Give the position of every malaria parasite and every leukocyte.
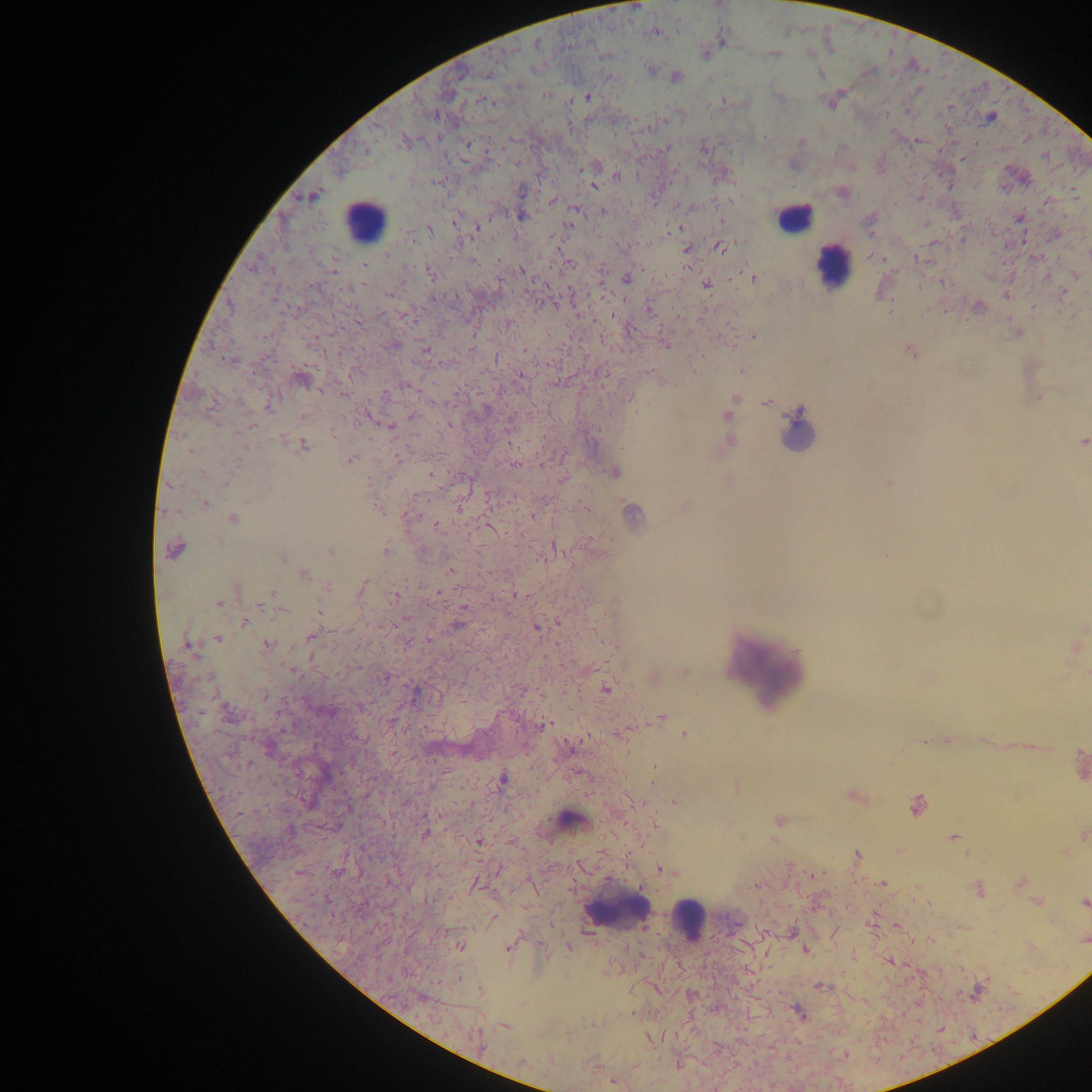
Approximate centers as x y in pixels.
Malaria parasites: 635 7; 655 32; 723 40; 537 44; 705 53; 810 53; 775 54; 650 69; 820 74; 676 77; 918 90; 547 95; 778 96; 588 97; 484 101; 830 103; 990 118; 800 142; 468 144; 618 177; 594 185; 522 191; 842 192; 311 196; 681 205; 575 209; 602 212; 522 216; 457 221; 870 224; 568 226; 478 227; 674 228; 429 230; 720 247; 686 251; 388 254; 473 261; 569 263; 364 265; 333 271; 430 272; 522 272; 1076 275; 626 278; 753 278; 943 283; 706 284; 390 293; 1006 295; 230 307; 406 316; 358 321; 509 324; 752 336; 396 345; 665 345; 425 349; 526 350; 912 351; 497 358; 230 361; 302 380; 519 380; 405 385; 344 396; 1038 398; 734 399; 240 402; 766 402; 270 406; 727 415; 412 416; 302 417; 251 426; 387 426; 282 440; 730 441; 1082 443; 303 445; 190 451; 400 458; 351 459; 515 464; 615 471; 202 472; 430 474; 728 480; 225 482; 369 482; 888 482; 204 503; 460 507; 685 507; 377 509; 632 513; 233 519; 438 526; 174 549; 330 551; 386 552; 282 558; 449 571; 304 575; 327 588; 361 588; 238 590; 438 592; 272 593; 396 595; 516 595; 219 603; 463 607; 318 611; 244 623; 457 625; 537 627; 310 637; 218 639; 428 640; 268 644; 187 645; 1077 646; 293 671; 685 671; 385 677; 654 679; 605 690; 414 694; 265 697; 661 717; 542 726; 622 734; 685 735; 569 748; 1080 761; 654 768; 502 780; 853 795; 675 802; 916 805; 778 820; 654 825; 424 833; 1083 836; 953 838; 773 841; 478 842; 856 855; 663 870; 882 883; 1020 883; 475 884; 756 886; 979 890; 1084 902; 1038 903; 460 946; 569 947; 507 948; 805 950; 820 986; 479 991; 798 1012; 505 1026; 476 1039; 650 1039; 678 1065; 614 1083.
Leukocytes: 793 217; 363 221; 831 268; 769 665; 572 819; 618 910; 690 920.

Thick blood film. Image is 1092×1092 pixels. Single field of view. Collected in Ghana. Photographed through a microscope with a mobile-phone camera.